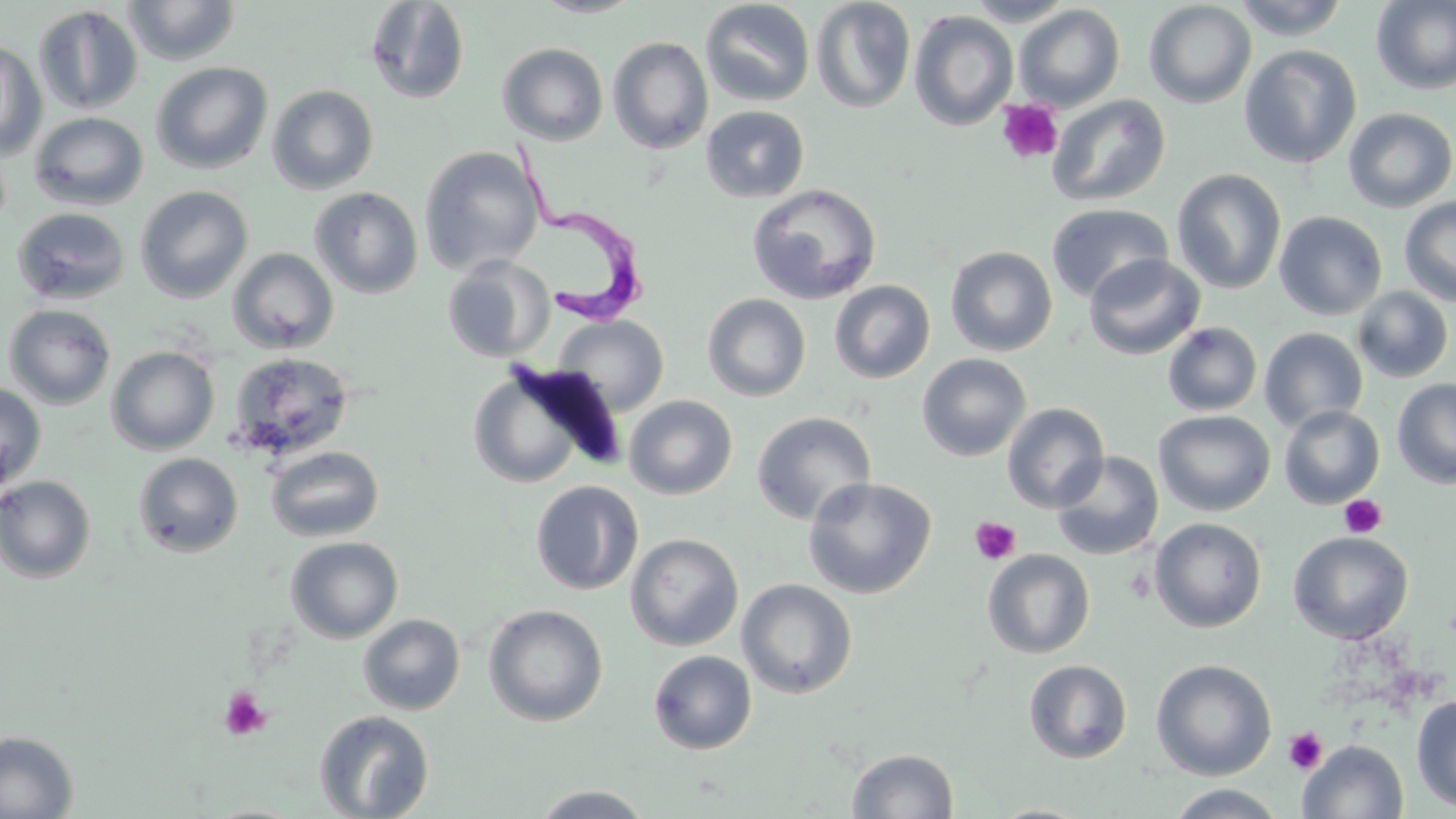
Approximate bounding boxes as (x1, y1, x2, y2) in pixels. Uninfected red blood cell locations: (122, 0, 241, 66), (530, 0, 645, 18), (810, 0, 916, 113), (962, 0, 1077, 26), (1231, 0, 1350, 40), (1370, 0, 1456, 96), (364, 1, 470, 105), (700, 1, 816, 107), (1143, 1, 1256, 109), (33, 4, 144, 115), (1013, 4, 1126, 112), (909, 10, 1018, 131), (607, 36, 713, 154), (0, 41, 47, 161), (496, 42, 609, 145), (1239, 44, 1362, 168), (150, 61, 273, 174), (266, 84, 380, 195), (1046, 94, 1171, 208), (700, 105, 810, 203), (1343, 107, 1456, 212), (29, 111, 148, 211), (419, 146, 544, 276), (1171, 168, 1286, 294), (747, 183, 882, 305), (135, 186, 253, 303), (309, 186, 424, 299), (1399, 196, 1456, 306), (1046, 203, 1173, 303), (12, 207, 131, 305), (1274, 210, 1388, 320), (945, 245, 1058, 357), (227, 247, 339, 354), (1082, 253, 1205, 360), (442, 257, 554, 362), (829, 280, 935, 383), (1351, 287, 1454, 383), (702, 293, 811, 401), (3, 304, 116, 410), (554, 315, 669, 415), (1161, 322, 1263, 416), (1258, 327, 1368, 433), (106, 346, 220, 455), (227, 352, 355, 461), (917, 353, 1031, 461), (467, 363, 616, 491), (1392, 379, 1456, 489), (0, 381, 47, 492), (624, 395, 738, 499), (1002, 402, 1109, 512), (1279, 405, 1385, 509), (1153, 410, 1275, 516), (751, 412, 877, 525), (265, 445, 384, 542), (1050, 451, 1165, 560), (133, 452, 243, 557), (0, 474, 97, 583), (802, 476, 937, 599), (530, 480, 644, 595), (1149, 517, 1267, 633), (1288, 531, 1413, 644), (625, 533, 743, 651), (285, 536, 404, 643), (982, 549, 1095, 659), (736, 579, 857, 699), (483, 603, 608, 727), (357, 614, 466, 715), (648, 650, 757, 754), (1023, 659, 1133, 764), (1150, 659, 1277, 781), (1410, 694, 1456, 813), (314, 709, 434, 818), (0, 730, 80, 819), (1296, 740, 1409, 819), (846, 748, 959, 818), (531, 785, 655, 818), (1165, 785, 1287, 818), (986, 803, 1095, 818). Trypanosoma brucei locations: (504, 137, 649, 328). Platelet locations: (996, 99, 1064, 165), (1340, 494, 1387, 538), (969, 516, 1020, 565), (218, 686, 271, 740), (1284, 728, 1327, 774). Slide-level diagnosis: Trypanosoma brucei. Light microscopy. Thin blood film. May-Grünwald-Giemsa-stained preparation. Single field of view. Image is 1456×819 pixels. Captured at 1000x magnification.